Give the position of every leukocyte visible.
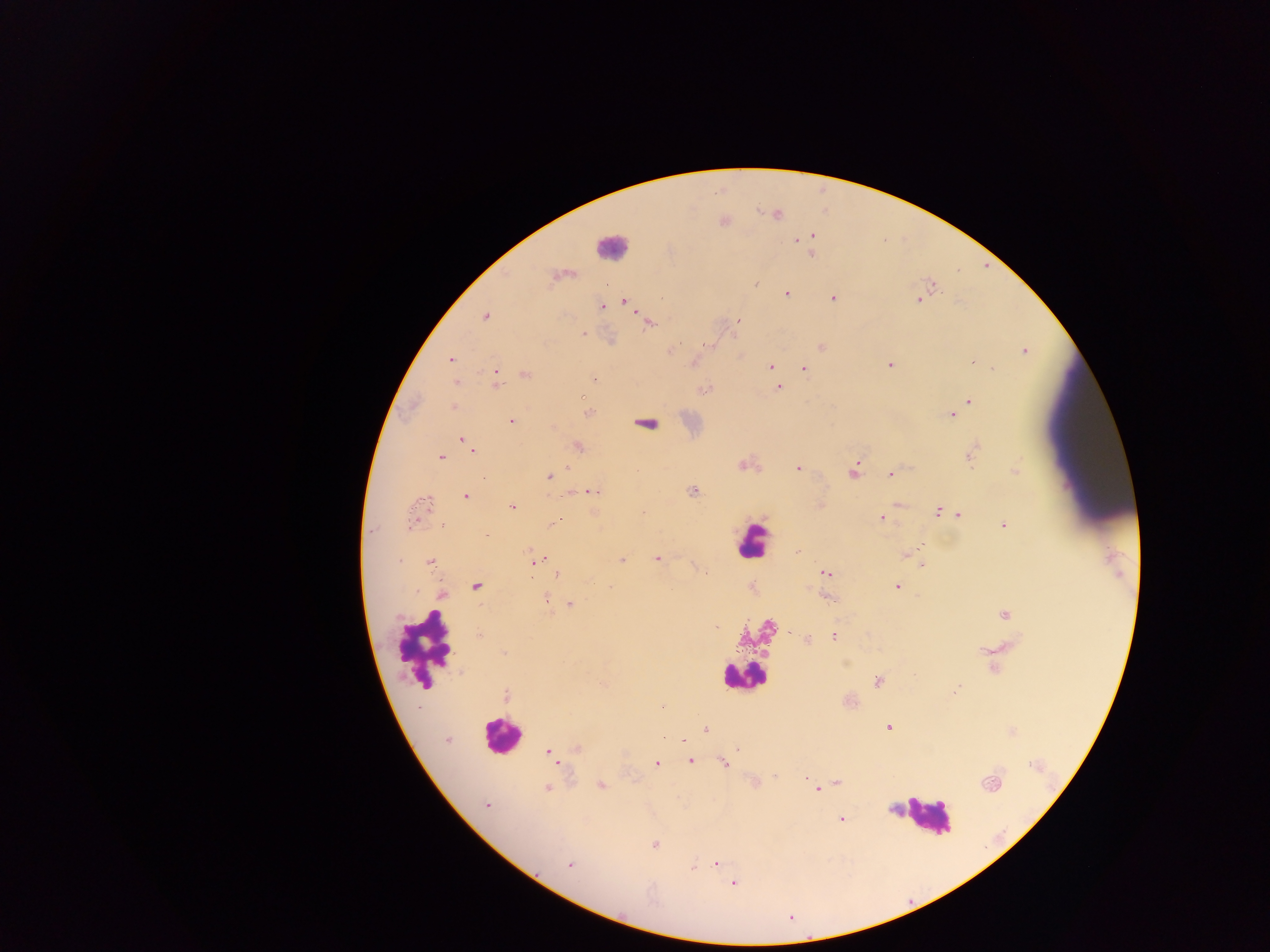
Approximate centers as {x, y} in pixels.
Leukocytes: {603, 247}, {758, 540}, {415, 647}, {740, 673}, {498, 735}, {924, 815}.

Summary:
  - Plasmodium parasite locations: {724, 222}, {811, 235}, {796, 242}, {812, 256}, {756, 281}, {786, 293}, {832, 297}, {661, 298}, {917, 299}, {623, 300}, {602, 306}, {485, 317}, {737, 321}, {649, 323}, {582, 332}, {821, 347}, {672, 351}, {1024, 353}, {450, 360}, {694, 360}, {971, 361}, {890, 364}, {770, 366}, {803, 369}, {990, 369}, {495, 370}, {595, 377}, {456, 381}, {496, 381}, {780, 387}, {970, 402}, {452, 407}, {950, 416}, {512, 421}, {463, 438}, {974, 446}, {578, 447}, {472, 452}, {971, 454}, {440, 455}, {742, 464}, {567, 467}, {798, 468}, {1015, 469}, {853, 471}, {892, 474}, {548, 476}, {691, 490}, {592, 491}, {466, 497}, {821, 501}, {423, 503}, {898, 504}, {513, 506}, {937, 512}, {959, 513}, {556, 519}, {881, 519}, {1003, 524}, {441, 526}, {919, 546}, {904, 554}, {535, 555}, {657, 558}, {538, 560}, {623, 560}, {431, 563}, {920, 564}, {533, 567}, {694, 568}, {826, 574}, {556, 575}, {897, 584}, {475, 586}, {546, 597}, {829, 598}, {569, 604}, {1004, 614}, {717, 627}, {834, 635}, {807, 639}, {980, 651}, {503, 654}, {846, 662}, {991, 669}, {877, 681}, {601, 683}, {955, 690}, {506, 694}, {662, 706}, {887, 725}, {706, 729}, {448, 740}, {681, 740}, {685, 743}, {575, 748}, {735, 748}, {546, 750}, {690, 761}, {723, 762}, {656, 764}, {774, 775}, {768, 777}, {803, 777}, {838, 782}, {753, 783}, {987, 784}, {600, 785}, {547, 788}, {817, 788}, {485, 804}, {841, 820}, {656, 844}, {717, 863}, {570, 864}, {693, 866}, {566, 867}, {733, 883}
  - Capture: mobile-phone photograph through a microscope
  - Field of view: single
  - Preparation: thick blood smear
  - Image size: 1270×952 pixels
  - Country: Ghana